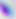
Micrograph. 400x magnification. Toxoplasma gondii is shown.